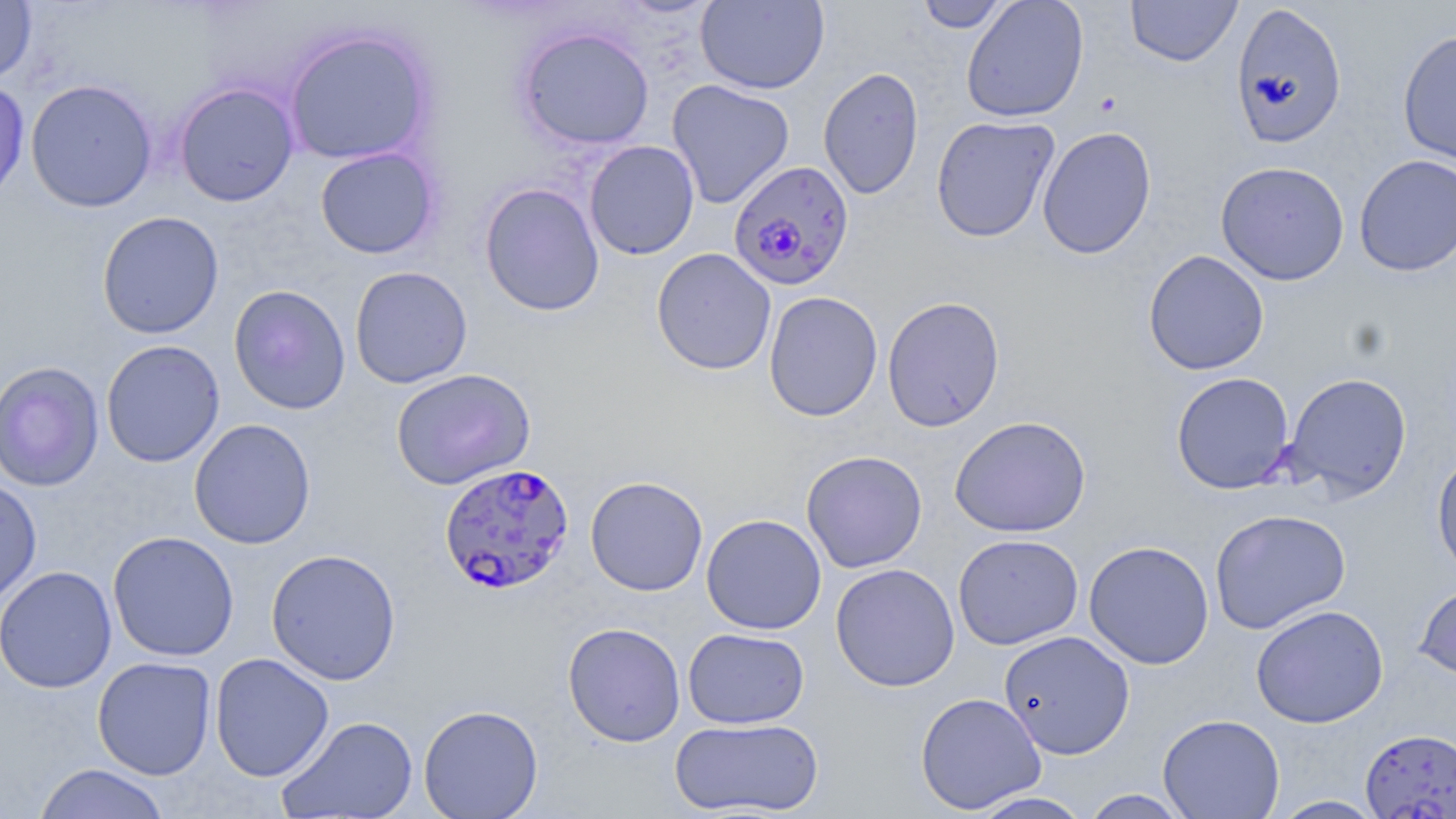
Approximate bounding boxes as (x1, y1, x2, y2) in pixels. Uninfected red blood cell locations: (916, 0, 1012, 33), (961, 0, 1089, 122), (1125, 0, 1242, 67), (695, 1, 830, 94), (0, 2, 37, 83), (1230, 3, 1347, 149), (515, 26, 655, 150), (284, 28, 435, 166), (1398, 29, 1456, 166), (818, 66, 924, 200), (25, 78, 158, 213), (0, 79, 30, 205), (667, 79, 795, 208), (173, 82, 300, 206), (931, 116, 1060, 242), (1037, 125, 1157, 260), (584, 140, 700, 260), (315, 147, 439, 259), (1354, 154, 1456, 276), (1215, 160, 1350, 285), (479, 182, 605, 316), (96, 211, 225, 339), (651, 248, 777, 375), (1143, 249, 1270, 376), (349, 266, 473, 388), (228, 285, 351, 415), (764, 291, 883, 422), (882, 295, 1005, 432), (101, 340, 225, 468), (0, 361, 105, 492), (391, 368, 536, 489), (1171, 371, 1294, 494), (1281, 371, 1413, 500), (949, 415, 1092, 537), (189, 418, 316, 549), (801, 450, 927, 572), (1432, 450, 1456, 582), (585, 476, 708, 596), (0, 478, 41, 607), (1209, 508, 1351, 635), (701, 514, 827, 634), (107, 531, 239, 661), (953, 533, 1084, 650), (1084, 540, 1215, 669), (265, 548, 402, 685), (830, 563, 960, 692), (0, 566, 117, 693), (1414, 580, 1456, 684), (1251, 604, 1388, 728), (562, 622, 686, 746), (683, 627, 809, 729), (998, 630, 1135, 760), (209, 653, 334, 782), (92, 656, 217, 780), (914, 692, 1047, 814), (418, 704, 544, 819), (1158, 713, 1285, 819), (277, 715, 418, 818), (669, 717, 825, 817), (1360, 728, 1455, 819), (32, 763, 172, 819), (1080, 789, 1194, 818), (966, 790, 1096, 819), (1269, 796, 1388, 818). Plasmodium falciparum-infected red blood cell locations: (728, 159, 855, 291), (438, 462, 575, 596). Slide-level diagnosis: Plasmodium falciparum. May-Grünwald-Giemsa stain. Thin blood smear. Light microscopy. Captured at 1000x magnification. Image is 1456×819 pixels. One field of a larger specimen.